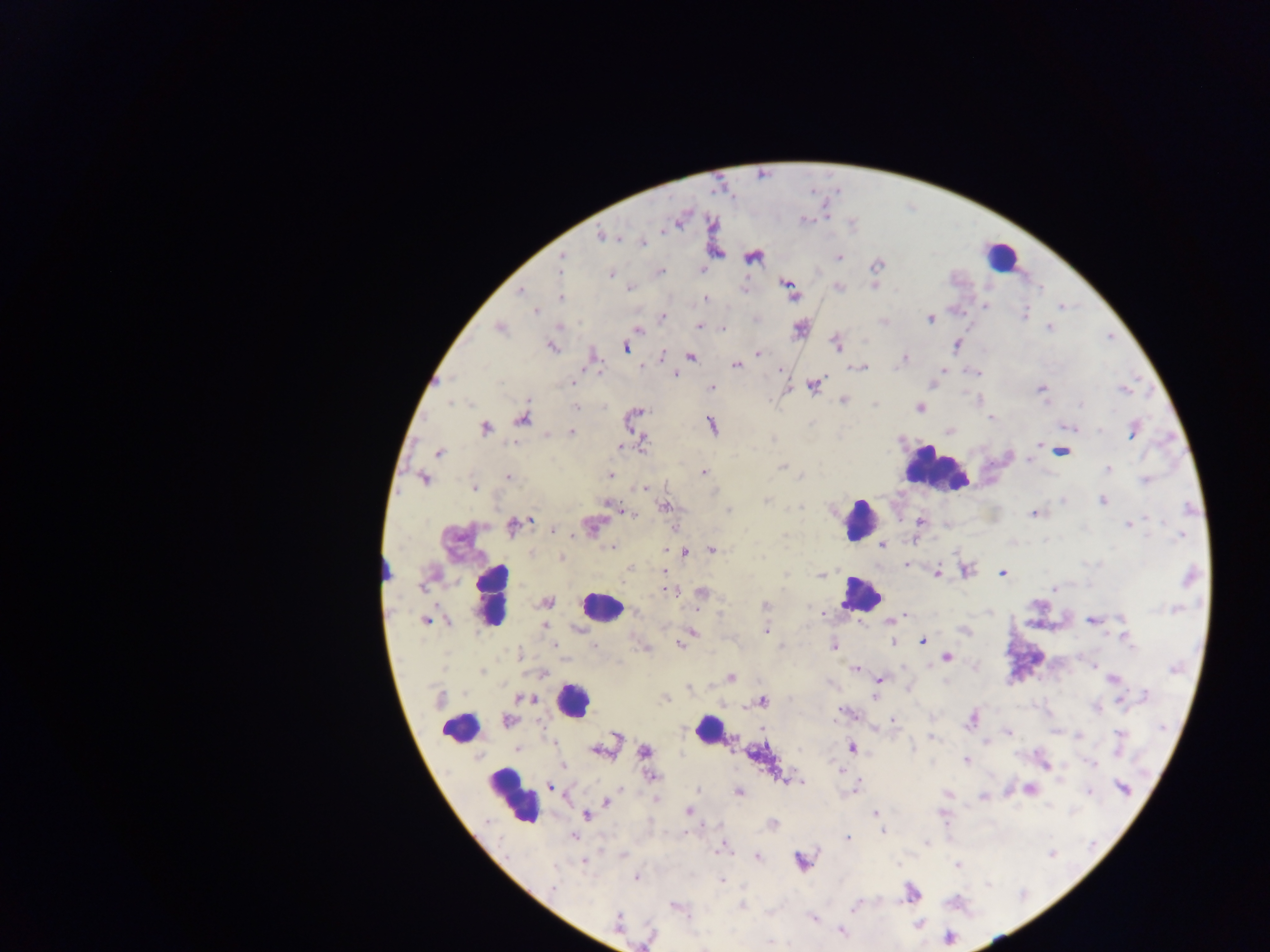
Approximate centers as {x, y} in pixels.
Summary:
  - Leukocyte locations: {1001, 257}, {934, 468}, {859, 519}, {383, 569}, {491, 595}, {860, 595}, {601, 609}, {572, 700}, {459, 727}, {708, 728}, {512, 795}
  - Malaria parasite locations: {680, 219}, {602, 236}, {642, 243}, {563, 256}, {752, 256}, {838, 257}, {877, 263}, {702, 268}, {660, 272}, {611, 274}, {787, 284}, {874, 285}, {839, 287}, {630, 288}, {520, 292}, {790, 293}, {560, 297}, {706, 298}, {985, 305}, {1060, 306}, {536, 310}, {1025, 314}, {661, 317}, {930, 319}, {884, 321}, {700, 326}, {722, 327}, {498, 328}, {800, 328}, {1049, 328}, {638, 330}, {836, 344}, {957, 345}, {551, 346}, {626, 348}, {757, 353}, {690, 355}, {592, 356}, {661, 356}, {904, 358}, {736, 365}, {640, 366}, {859, 367}, {781, 368}, {943, 369}, {675, 373}, {977, 373}, {573, 384}, {930, 384}, {813, 385}, {712, 387}, {1041, 389}, {1124, 389}, {843, 400}, {575, 407}, {919, 407}, {992, 417}, {522, 418}, {633, 418}, {710, 424}, {1067, 426}, {484, 428}, {1134, 429}, {949, 430}, {572, 432}, {642, 441}, {1038, 442}, {621, 447}, {1061, 451}, {438, 452}, {1028, 459}, {781, 466}, {1107, 469}, {702, 472}, {609, 475}, {508, 477}, {423, 478}, {1146, 480}, {473, 486}, {644, 487}, {766, 501}, {1102, 501}, {609, 502}, {664, 506}, {726, 511}, {628, 513}, {1034, 513}, {919, 521}, {513, 525}, {591, 525}, {1129, 525}, {674, 527}, {553, 529}, {1180, 536}, {883, 544}, {885, 546}, {613, 547}, {665, 550}, {684, 550}, {711, 550}, {560, 558}, {906, 564}, {630, 567}, {965, 569}, {937, 573}, {1002, 573}, {820, 575}, {1054, 588}, {668, 590}, {701, 593}, {546, 602}, {766, 605}, {822, 613}, {905, 614}, {895, 618}, {426, 620}, {1092, 620}, {889, 621}, {544, 624}, {964, 629}, {764, 630}, {691, 632}, {1125, 635}, {923, 640}, {892, 641}, {679, 643}, {554, 645}, {592, 645}, {834, 645}, {644, 646}, {947, 657}, {856, 669}, {541, 673}, {730, 678}, {1113, 679}, {878, 680}, {666, 698}, {527, 699}, {761, 701}, {1095, 708}, {972, 718}, {893, 720}, {508, 721}, {1008, 732}, {1119, 733}, {931, 735}, {986, 743}, {604, 747}, {852, 747}, {518, 749}, {645, 751}, {966, 759}, {1044, 764}, {1091, 764}, {562, 765}, {651, 776}, {784, 779}, {796, 781}, {550, 786}, {855, 787}, {1123, 787}, {620, 788}, {1029, 788}, {698, 791}, {739, 791}, {948, 794}, {983, 796}, {656, 798}, {606, 802}, {688, 810}, {875, 813}, {586, 814}, {772, 825}, {883, 829}, {574, 836}, {846, 837}, {721, 849}, {757, 856}, {583, 861}, {801, 861}, {957, 864}, {636, 877}, {721, 880}, {912, 892}, {675, 905}, {741, 906}, {812, 918}, {618, 922}, {840, 930}, {702, 946}
  - Preparation: thick blood smear
  - Country: Ghana
  - Field of view: single
  - Capture: mobile-phone photograph through a microscope
  - Image size: 1270×952 pixels